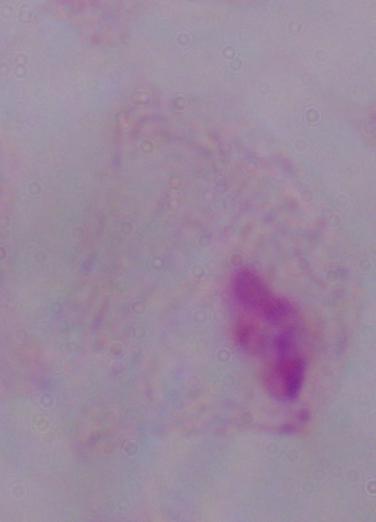
Summary:
  - Modality: micrograph
  - Identification: trichomonad
  - Magnification: 1000x